Outline each blood parasite and name the species.
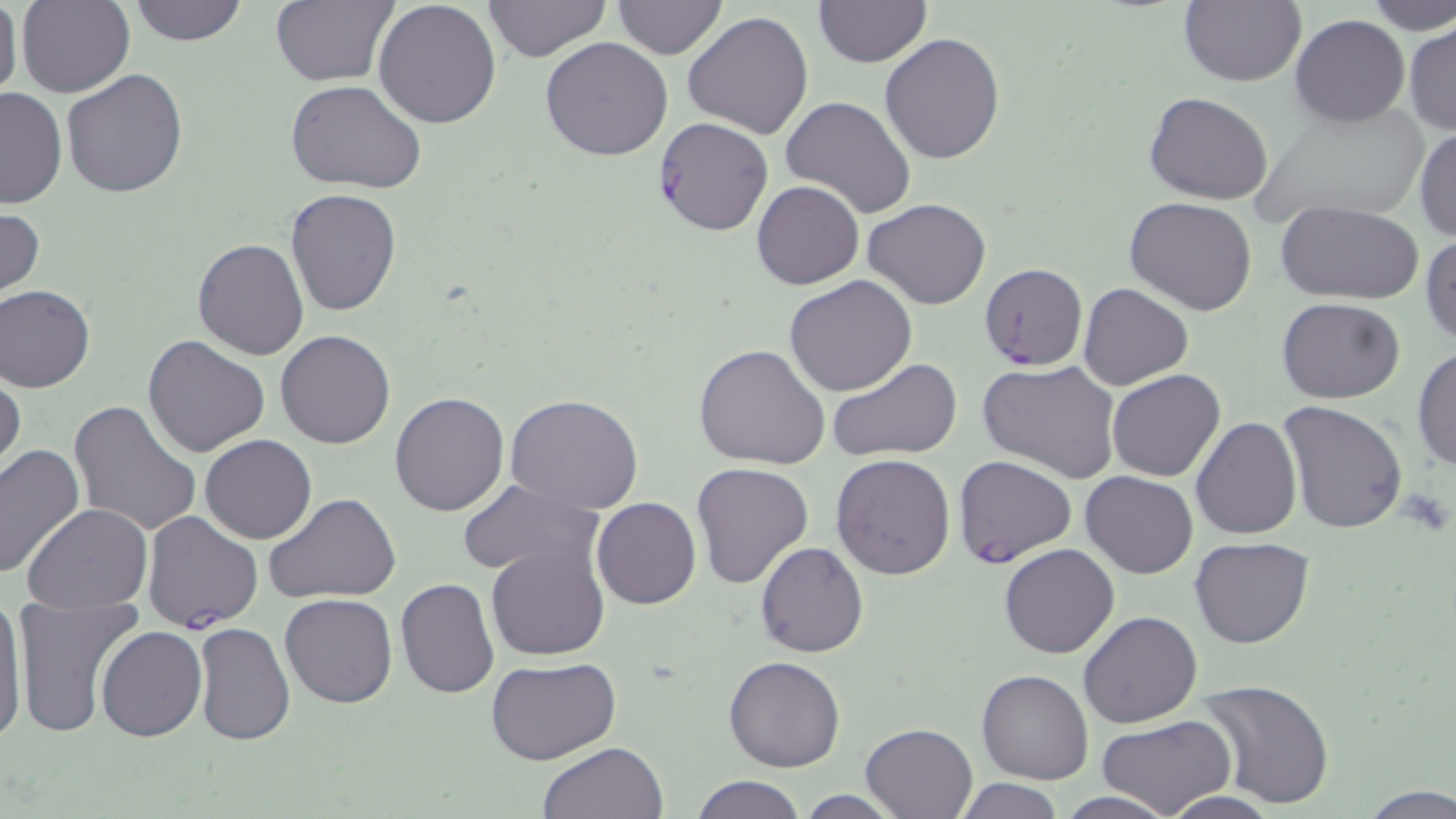

Approximate bounding boxes as [x1, y1, x2, y2] in pixels.
Plasmodium falciparum-infected red blood cells: [653, 116, 773, 238], [979, 261, 1088, 372], [951, 455, 1077, 570], [142, 511, 263, 634].
No Plasmodium ovale, Plasmodium malariae, Plasmodium vivax, Babesia divergens, or Trypanosoma brucei observed.

Summary:
  - Platelet locations: [1397, 488, 1452, 538]
  - Uninfected red blood cell locations: [17, 0, 133, 98], [125, 0, 251, 47], [271, 0, 399, 87], [482, 0, 611, 62], [612, 0, 729, 58], [813, 0, 930, 67], [1360, 0, 1456, 36], [372, 1, 502, 129], [1177, 1, 1306, 86], [0, 3, 23, 104], [684, 10, 814, 138], [1291, 15, 1408, 127], [1404, 21, 1456, 136], [880, 32, 1006, 163], [540, 37, 673, 160], [60, 68, 189, 197], [284, 80, 427, 193], [0, 86, 66, 210], [1143, 91, 1274, 204], [779, 96, 917, 221], [1241, 104, 1435, 229], [1414, 123, 1456, 240], [751, 180, 863, 290], [286, 188, 401, 317], [1124, 197, 1259, 316], [863, 200, 991, 310], [1274, 200, 1423, 304], [0, 205, 45, 305], [1421, 234, 1456, 347], [191, 237, 309, 359], [785, 276, 917, 397], [1078, 282, 1193, 390], [0, 284, 96, 393], [1277, 297, 1406, 402], [276, 329, 395, 448], [142, 336, 270, 457], [693, 343, 831, 469], [1412, 345, 1456, 473], [828, 358, 962, 461], [978, 358, 1122, 484], [1107, 369, 1225, 482], [0, 371, 25, 478], [390, 391, 509, 516], [504, 394, 645, 514], [68, 399, 203, 539], [1276, 402, 1408, 537], [1191, 416, 1302, 538], [200, 435, 317, 544], [0, 444, 85, 580], [831, 454, 955, 579], [690, 461, 814, 588], [1081, 471, 1198, 579], [458, 479, 604, 578], [267, 494, 401, 604], [592, 497, 701, 610], [24, 504, 154, 613], [1190, 537, 1314, 648], [754, 541, 869, 658], [486, 543, 610, 661], [999, 544, 1120, 659], [395, 578, 499, 699], [279, 593, 398, 709], [11, 595, 142, 737], [0, 596, 29, 747], [1079, 611, 1203, 729], [193, 622, 294, 747], [96, 626, 206, 741], [723, 655, 847, 772], [485, 657, 622, 766], [977, 670, 1093, 785], [1196, 679, 1335, 808], [1097, 714, 1237, 819], [859, 721, 980, 818], [538, 742, 669, 819], [690, 775, 806, 818], [952, 778, 1067, 818], [1360, 786, 1456, 817], [794, 792, 904, 818]
  - Slide-level diagnosis: Plasmodium falciparum
  - Preparation: thin blood film
  - Magnification: 1000x
  - Modality: light microscopy
  - Image size: 1456×819 pixels
  - Field of view: single
  - Stain: May-Grünwald-Giemsa